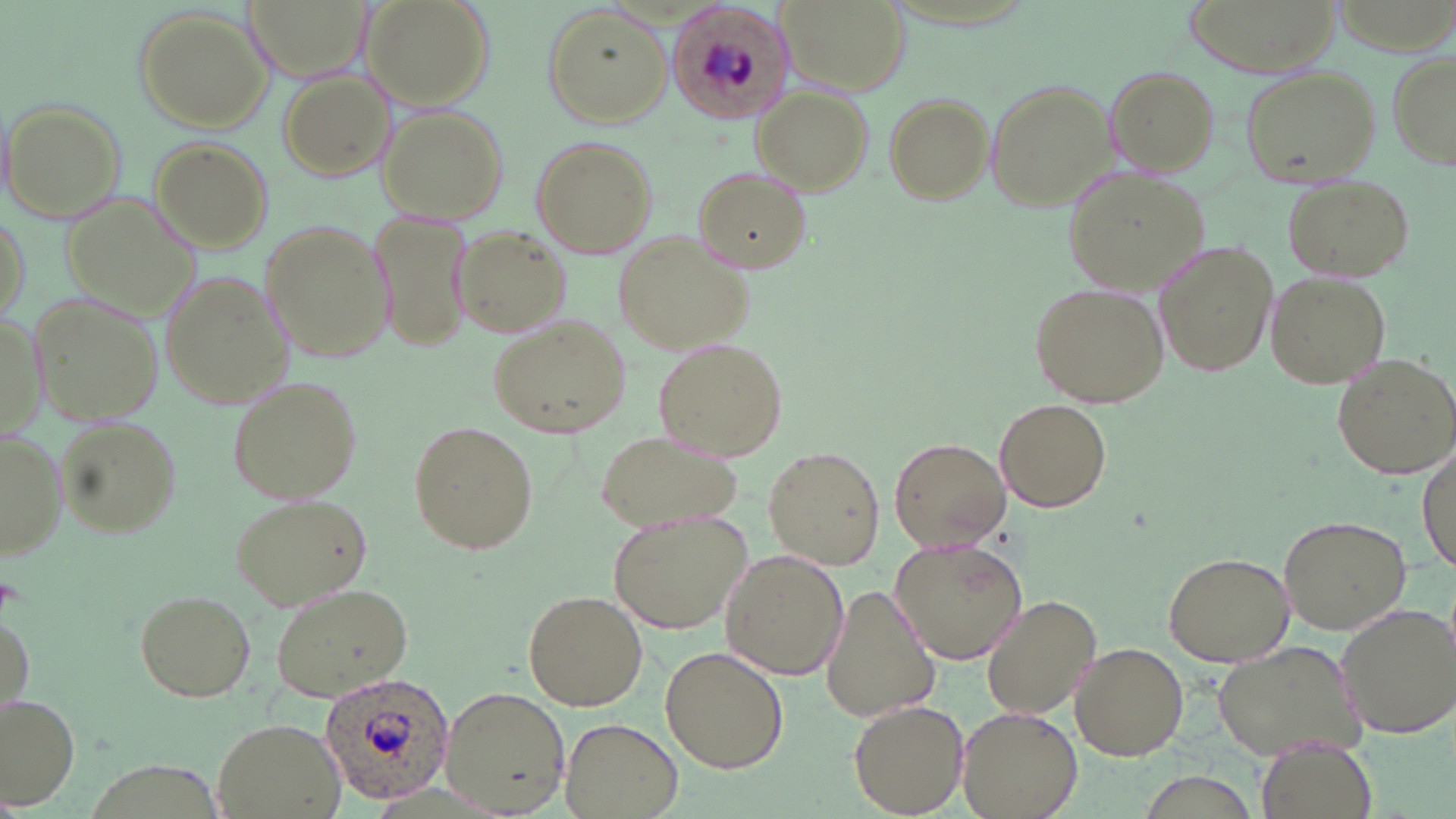
Approximate bounding boxes as (x1, y1, x2, y2) in pixels. Plasmodium ovale-infected red blood cell locations: (665, 3, 794, 122), (320, 670, 454, 803). Uninfected red blood cell locations: (360, 0, 493, 112), (777, 0, 914, 99), (1183, 0, 1338, 76), (541, 4, 670, 127), (136, 7, 272, 130), (238, 8, 385, 92), (1386, 52, 1456, 170), (1103, 64, 1220, 174), (1236, 64, 1384, 188), (279, 70, 396, 182), (983, 77, 1114, 210), (755, 88, 873, 194), (881, 93, 994, 207), (3, 100, 125, 223), (378, 106, 510, 224), (529, 133, 658, 257), (150, 138, 272, 252), (691, 166, 810, 274), (1068, 170, 1212, 296), (1282, 175, 1412, 282), (61, 190, 201, 330), (369, 208, 473, 348), (259, 220, 392, 366), (452, 225, 573, 341), (616, 230, 756, 353), (1152, 242, 1279, 379), (1266, 271, 1391, 388), (160, 272, 299, 409), (1032, 280, 1171, 407), (32, 293, 163, 422), (0, 308, 42, 447), (489, 316, 630, 440), (653, 338, 784, 461), (1328, 351, 1456, 479), (226, 375, 365, 504), (995, 398, 1113, 512), (58, 419, 181, 534), (410, 421, 537, 554), (593, 425, 742, 531), (0, 430, 67, 560), (889, 436, 1011, 550), (764, 445, 885, 570), (1416, 447, 1454, 571), (230, 492, 371, 610), (609, 510, 752, 635), (1277, 513, 1411, 633), (890, 533, 1029, 665), (719, 549, 849, 682), (1163, 550, 1295, 665), (822, 580, 940, 724), (266, 583, 411, 702), (132, 587, 255, 701), (524, 589, 648, 712), (980, 594, 1101, 720), (1334, 603, 1455, 738), (0, 606, 33, 720), (1211, 637, 1363, 763), (1069, 641, 1189, 760), (660, 644, 788, 773), (438, 686, 569, 815), (0, 693, 78, 808), (850, 700, 968, 817), (956, 706, 1081, 819), (210, 715, 345, 819), (559, 718, 683, 819), (1256, 736, 1375, 819). Slide-level diagnosis: Plasmodium ovale. Captured at 1000x magnification. Thin blood smear. Optical microscopy. One field of a larger specimen. Image is 1456×819 pixels. May-Grünwald-Giemsa-stained preparation.